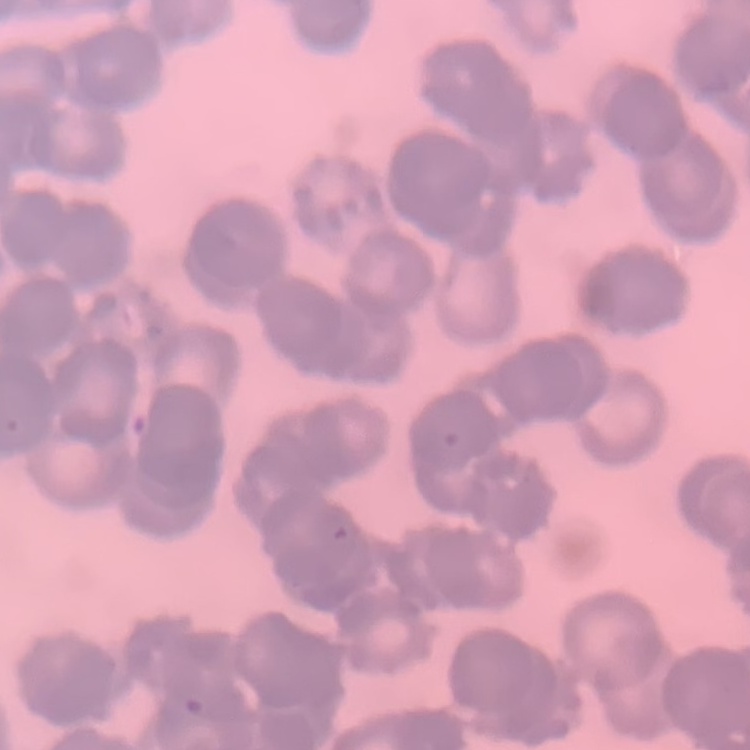

The red blood cells exhibit rouleaux formation. Square crop of a larger photomicrograph. Field's or Giemsa stain. Thin blood film.